Comment on the morphology of the erythrocytes.
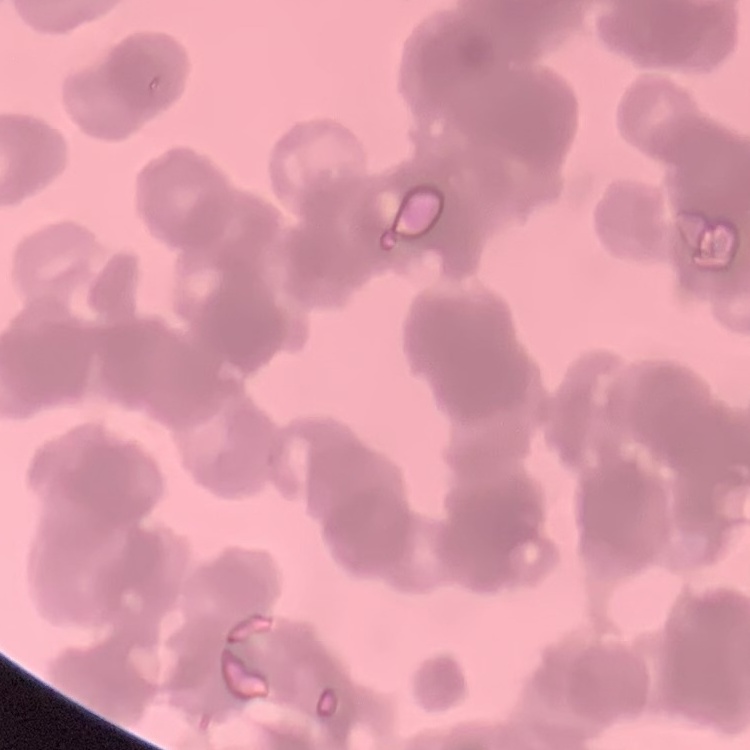

Rouleaux formation.

Summary:
  - Preparation: thin blood smear
  - Stain: Field's or Giemsa
  - Image type: one tile cut from a larger photomicrograph